Report the malaria status of this cell.
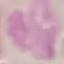

Uninfected.

{
  "image_type": "automatically extracted cell patch, resized to 64 × 64 pixels",
  "preparation": "thin blood smear",
  "capture": "smartphone camera at the microscope eyepiece",
  "stain": "Giemsa"
}